Describe the morphology of the erythrocytes.
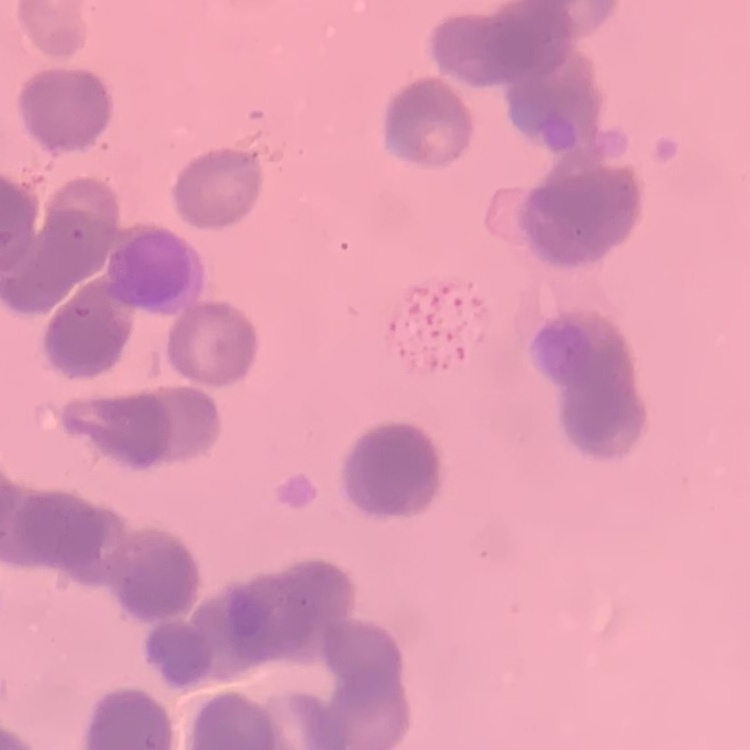

They show rouleaux formation.

Stained with either Field's or Giemsa. One tile cut from a larger photomicrograph. Thin peripheral smear.